Locate every Plasmodium falciparum parasite and give its life-cycle stage, and locate every leukocyte and any debris.
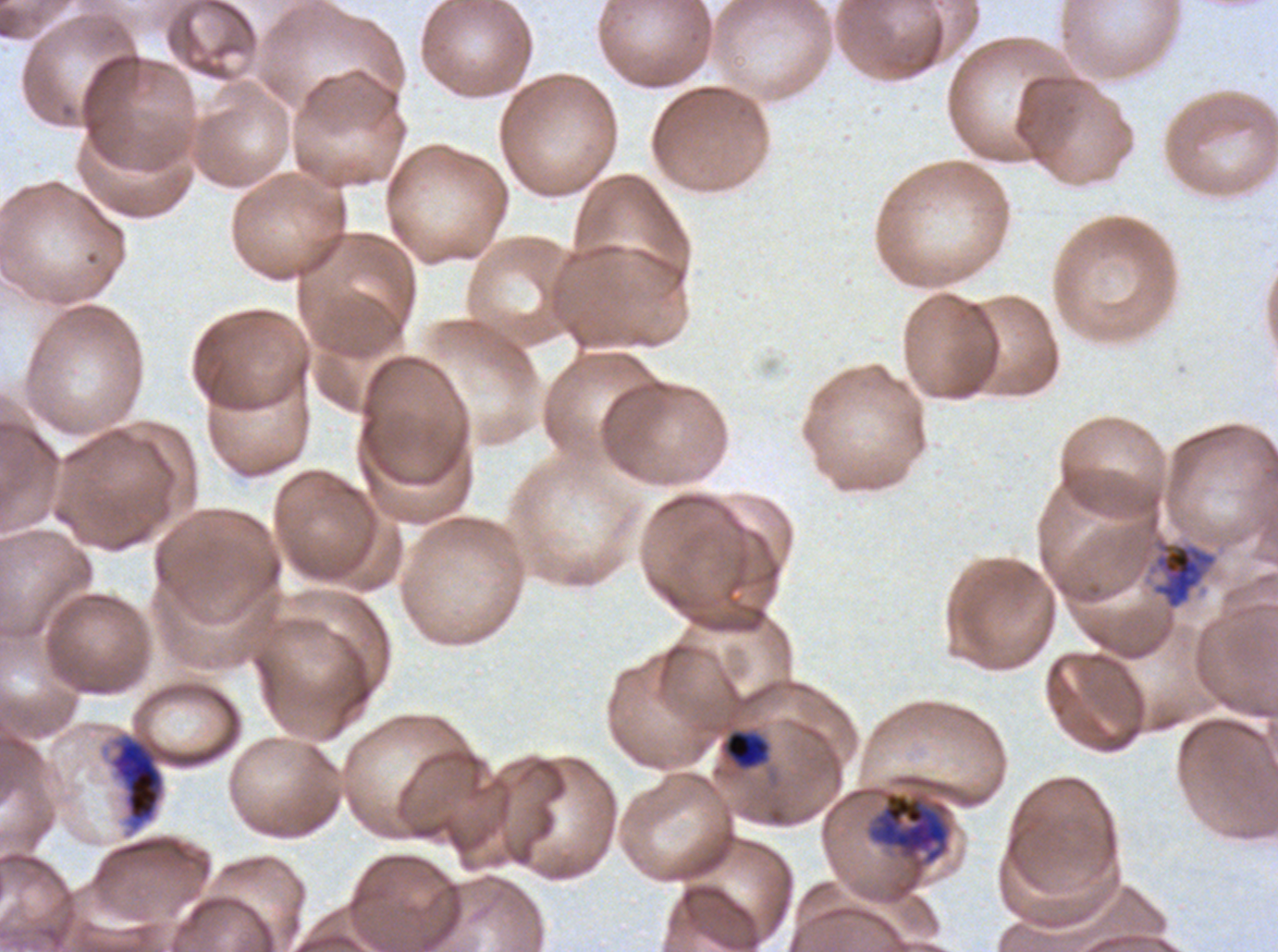
Approximate bounding boxes as {x1, y1, x2, y2} in pixels.
Late-ring/early-trophozoite forms: {724, 729, 769, 769}.
Late trophozoites: {1152, 542, 1217, 609}.
Early schizonts: {110, 737, 164, 824}, {868, 791, 950, 863}.
No rings, mid trophozoites, late schizonts, segmenters, gametocytes, leukocytes, or debris observed.

Image is 1278×952 pixels. A sub-image separated from a larger composite. Giemsa-stained preparation. Life-cycle stages observed: late-ring/early-trophozoite, late trophozoite, early schizont. Plasmodium falciparum from a patient in The Gambia, cultured ex vivo for 24 to 48 hours. Thin blood film.